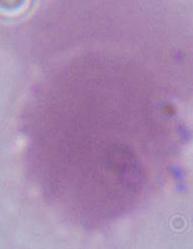
{
  "identification": "erythrocyte",
  "modality": "micrograph",
  "magnification": "1000x"
}